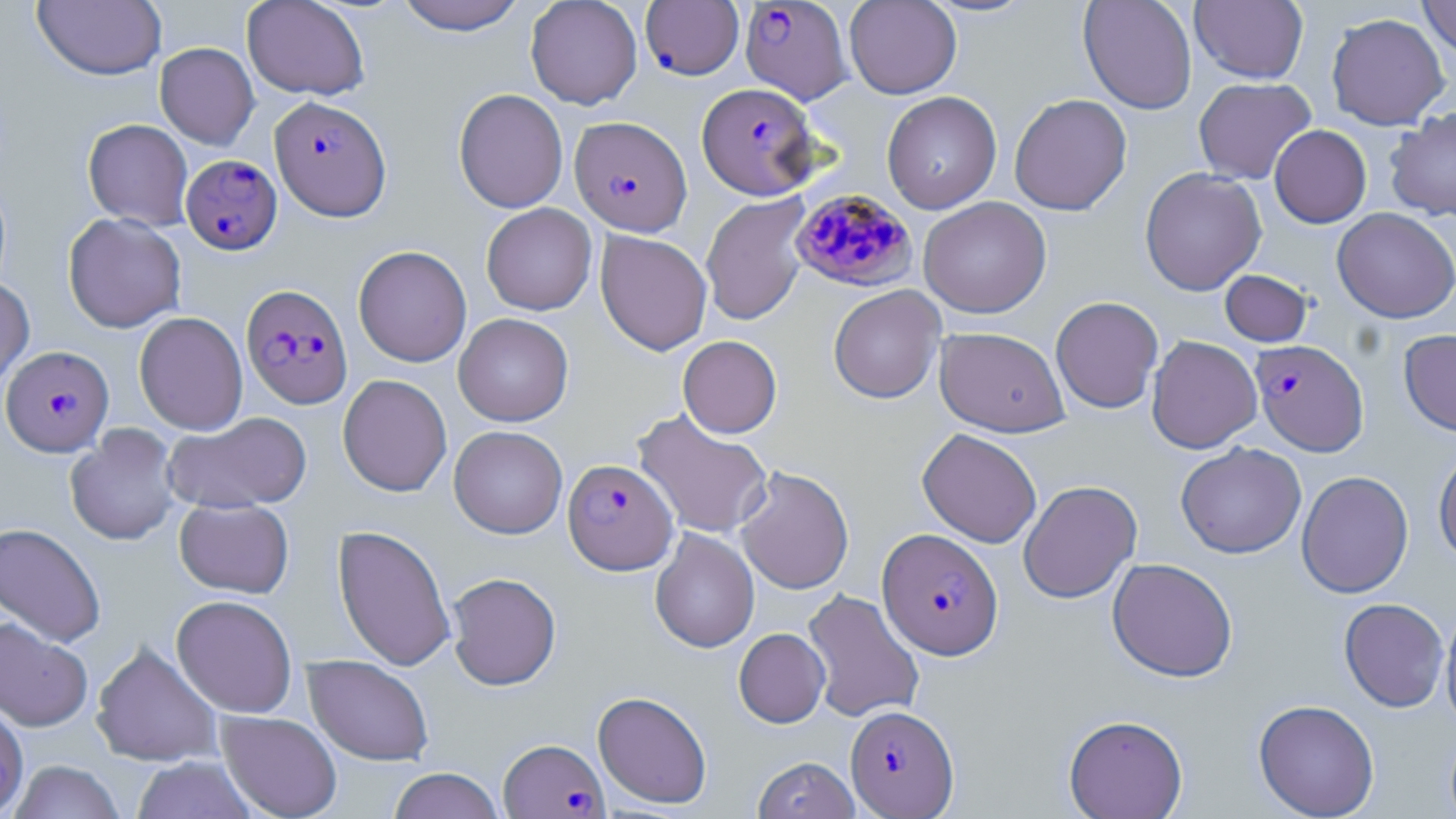

slide_level_diagnosis: Plasmodium falciparum
uninfected_red_blood_cell_locations_subset: 'approximate bounding boxes as (x1,y1)-(x2,y2) corner pairs in pixels: (242,0)-(370,101), (392,0)-(528,34), (525,0)-(643,109), (844,0)-(962,99), (920,0)-(1040,18), (1078,0)-(1197,115), (1191,0)-(1308,83), (1418,0)-(1456,61), (32,1)-(167,81), (1326,13)-(1450,130), (155,42)-(259,149), (1193,77)-(1316,184), (453,88)-(568,213), (882,91)-(1002,214), (1009,93)-(1132,216), (1385,107)-(1456,221), (82,119)-(193,230), (1269,124)-(1372,228), (1140,167)-(1266,296), (700,194)-(811,326), (918,196)-(1051,318), (481,203)-(597,315), (1332,208)-(1456,323), (63,213)-(186,333), (595,230)-(712,355), (353,245)-(472,367), (1220,270)-(1312,347), (0,277)-(35,390), (828,285)-(945,403), (1051,296)-(1164,414), (134,312)-(248,435), (453,313)-(574,426), (934,327)-(1069,437), (1398,328)-(1456,437), (677,335)-(782,438), (1146,335)-(1262,454), (337,374)-(452,497), (632,409)-(774,539), (162,411)-(311,514), (65,424)-(181,545), (449,425)-(567,538), (917,428)-(1042,548), (1175,442)-(1307,558), (1433,444)-(1456,565), (736,466)-(854,594), (1296,470)-(1414,598), (1018,479)-(1142,604), (174,498)-(294,598), (0,522)-(107,647), (332,524)-(455,671), (650,528)-(760,653), (1107,557)-(1238,682), (446,572)-(561,690), (802,589)-(925,723), (171,594)-(297,718), (1339,598)-(1450,712), (1440,604)-(1456,730), (0,618)-(93,731), (734,628)-(830,727), (91,641)-(223,767), (303,655)-(434,766), (593,691)-(712,808), (1253,699)-(1380,818), (216,711)-(342,819), (1064,714)-(1188,819), (132,755)-(258,818), (752,756)-(860,819), (9,760)-(124,819), (387,768)-(504,819)'
field_of_view: single
modality: optical microscopy
image_size: 1456×819 pixels
plasmodium_falciparum_infected_red_blood_cell_locations_subset: 'approximate bounding boxes as (x1,y1)-(x2,y2) corner pairs in pixels: (739,0)-(852,104), (642,1)-(746,80), (697,82)-(820,200), (270,96)-(391,220), (570,116)-(691,236), (180,154)-(282,254), (790,188)-(918,292), (241,284)-(353,409), (1250,339)-(1369,456), (1,345)-(114,456), (562,459)-(678,574), (877,528)-(1003,660), (845,704)-(959,817), (498,737)-(608,818)'
stain: May-Grünwald-Giemsa
preparation: thin blood smear
magnification: 1000x